Give the position of every leukocyte visible.
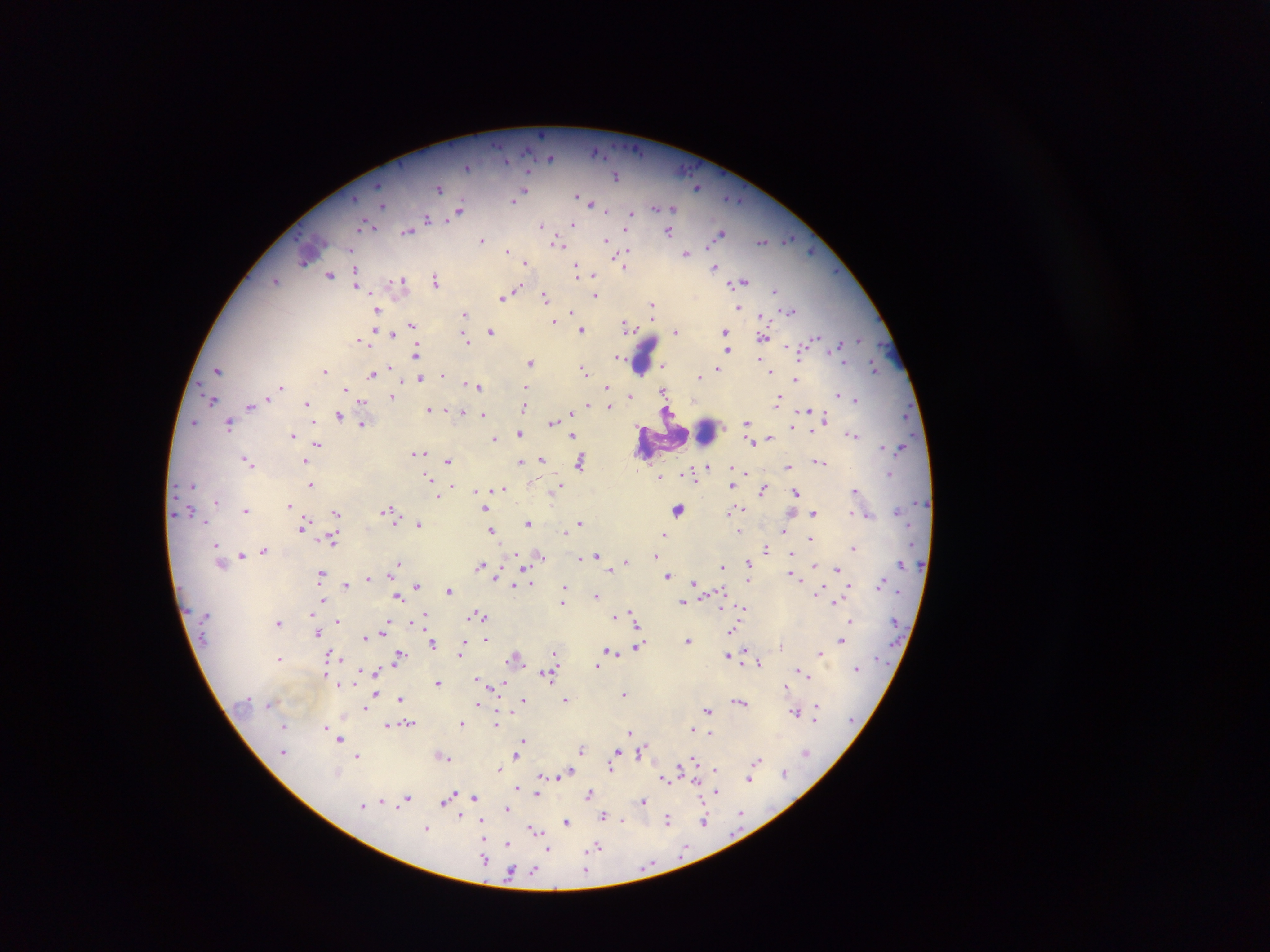

Approximate centers as x y in pixels.
Leukocytes: 643 358; 703 432; 676 510.

Summary:
  - Malaria parasite locations: 541 134; 596 151; 550 157; 506 161; 467 167; 616 176; 697 187; 439 188; 523 192; 576 195; 515 200; 591 203; 382 204; 656 208; 672 208; 459 210; 606 211; 631 214; 450 217; 428 218; 573 224; 364 225; 542 225; 627 228; 408 231; 668 232; 720 233; 788 239; 482 240; 606 240; 763 241; 558 243; 352 250; 508 251; 686 253; 625 255; 622 261; 303 262; 526 262; 577 267; 625 267; 715 267; 356 274; 330 275; 593 275; 276 280; 402 280; 436 280; 743 282; 356 284; 517 290; 775 291; 595 295; 504 296; 545 297; 652 305; 738 308; 376 309; 791 311; 571 312; 464 314; 762 316; 652 318; 554 321; 412 325; 628 325; 374 330; 582 330; 724 330; 491 331; 676 332; 392 335; 763 337; 815 339; 360 340; 466 340; 858 340; 840 344; 788 346; 727 351; 416 354; 617 356; 760 360; 530 362; 844 362; 719 365; 390 367; 662 367; 874 368; 717 369; 219 370; 583 370; 325 371; 770 371; 373 373; 443 375; 699 376; 420 379; 796 379; 466 384; 281 386; 479 386; 525 387; 607 387; 346 390; 663 391; 839 394; 630 396; 778 396; 390 397; 267 399; 212 400; 856 400; 363 401; 307 403; 250 407; 523 407; 609 407; 429 410; 449 410; 806 410; 463 412; 339 415; 483 415; 826 417; 193 422; 552 422; 747 423; 230 424; 362 424; 792 426; 812 431; 519 433; 852 435; 292 436; 573 436; 493 438; 769 438; 752 443; 318 445; 883 446; 419 454; 541 459; 247 461; 449 461; 580 461; 305 462; 519 462; 820 462; 707 465; 788 467; 746 472; 890 474; 692 475; 428 477; 660 477; 311 484; 192 485; 557 486; 451 487; 731 487; 502 488; 855 489; 763 490; 475 491; 796 492; 438 495; 216 501; 289 505; 388 509; 246 510; 485 510; 742 510; 730 511; 336 513; 814 513; 852 513; 869 515; 579 522; 528 523; 419 525; 303 526; 491 530; 739 531; 782 531; 564 533; 663 534; 811 538; 333 541; 216 546; 766 548; 854 548; 264 550; 790 553; 241 555; 596 555; 541 556; 655 556; 581 558; 626 561; 748 562; 397 564; 480 565; 814 565; 722 566; 838 568; 395 569; 609 571; 498 572; 392 573; 320 574; 668 575; 791 575; 368 578; 695 582; 530 583; 880 583; 346 585; 514 585; 849 585; 416 586; 565 588; 449 591; 597 596; 397 598; 322 601; 562 602; 683 602; 834 602; 744 609; 478 614; 424 615; 614 616; 633 616; 852 620; 338 621; 412 621; 279 622; 636 623; 384 630; 732 631; 316 634; 365 637; 486 638; 687 639; 841 641; 433 643; 638 645; 781 645; 461 648; 745 649; 610 650; 460 652; 554 653; 820 653; 400 655; 728 655; 333 656; 516 657; 280 659; 758 663; 597 667; 856 669; 376 671; 800 671; 548 674; 806 675; 477 677; 438 683; 341 684; 503 684; 787 686; 376 693; 624 693; 401 699; 524 700; 566 700; 741 702; 270 705; 478 705; 366 707; 707 709; 816 711; 796 712; 461 723; 409 724; 496 724; 388 725; 284 726; 326 727; 693 729; 332 730; 630 731; 710 734; 634 737; 339 739; 524 740; 581 748; 616 751; 641 751; 284 752; 806 752; 358 755; 444 756; 516 757; 694 760; 757 761; 611 767; 500 769; 680 769; 715 769; 784 771; 337 772; 570 772; 541 775; 564 775; 665 779; 750 779; 518 788; 717 792; 589 793; 536 794; 475 797; 408 798; 447 799; 381 801; 643 802; 363 805; 507 809; 741 814; 604 815; 458 816; 668 820; 622 821; 705 821; 481 822; 567 822; 427 828; 534 829; 508 844; 596 847; 548 849; 484 858; 586 869; 534 871; 510 872
  - Capture: mobile-phone photograph through a microscope
  - Field of view: single
  - Image size: 1270×952 pixels
  - Preparation: thick blood film
  - Country: Ghana